Assess the morphology of the erythrocytes.
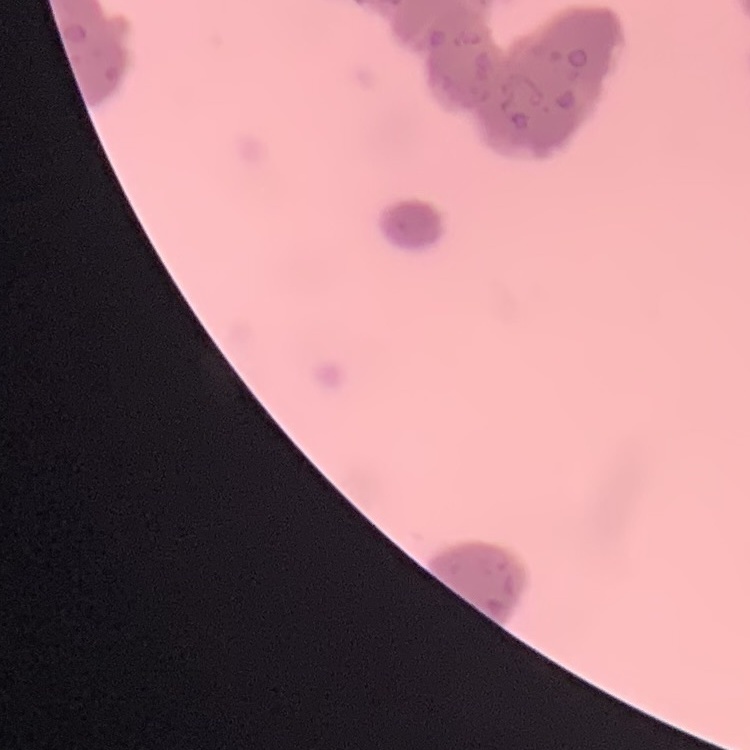
They show rouleaux formation.

Summary:
  - Image type: one tile cut from a larger photomicrograph
  - Preparation: thin blood smear
  - Stain: Field's or Giemsa